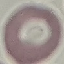

result = no malaria parasites detected
stain = Giemsa
image type = cell patch, automatically extracted from a larger field of view and resized to 64 × 64 pixels
capture = smartphone camera at the microscope eyepiece
preparation = thin blood film